Assess this cell for malaria.
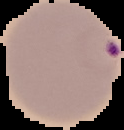
It is parasitized.

Summary:
  - Image type: cell region segmented out of the field of view; surrounding area masked to black
  - Image size: 124×130 pixels
  - Preparation: thin blood smear